Point out each Plasmodium parasite and each leukocyte.
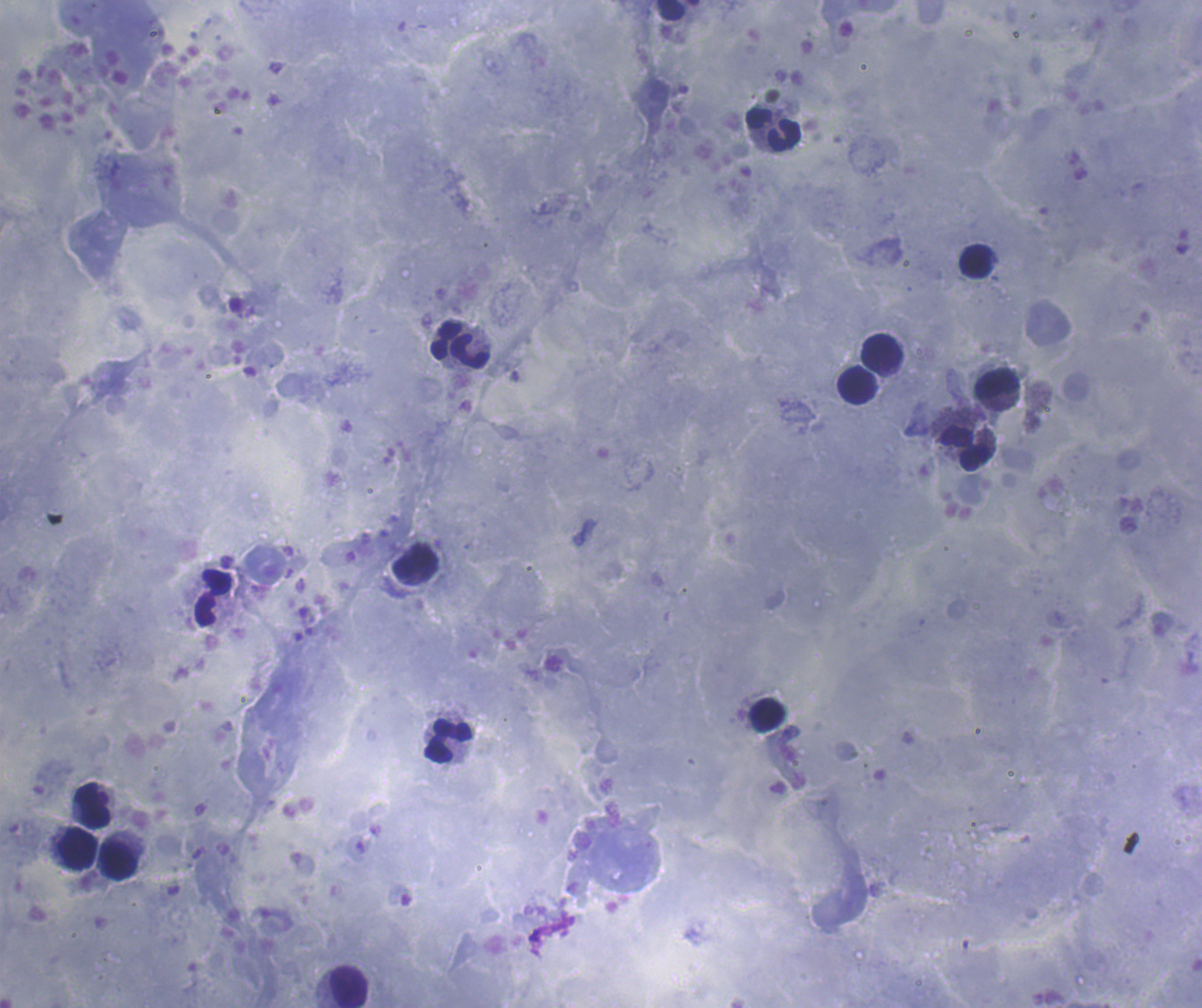
No Plasmodium parasites detected.
Approximate centers as {x, y} in pixels.
Leukocytes: {668, 10}, {772, 128}, {976, 261}, {444, 340}, {469, 351}, {882, 353}, {997, 384}, {858, 385}, {965, 449}, {213, 597}, {768, 714}, {449, 740}, {92, 805}, {78, 850}, {118, 860}, {349, 987}.

100x magnification. Thick blood smear. Romanowsky-stained preparation. Image is 1202×1008 pixels. Coloration quality: good. One field from this slide. Previously used in an actual diagnosis. Background quality: satisfactory.